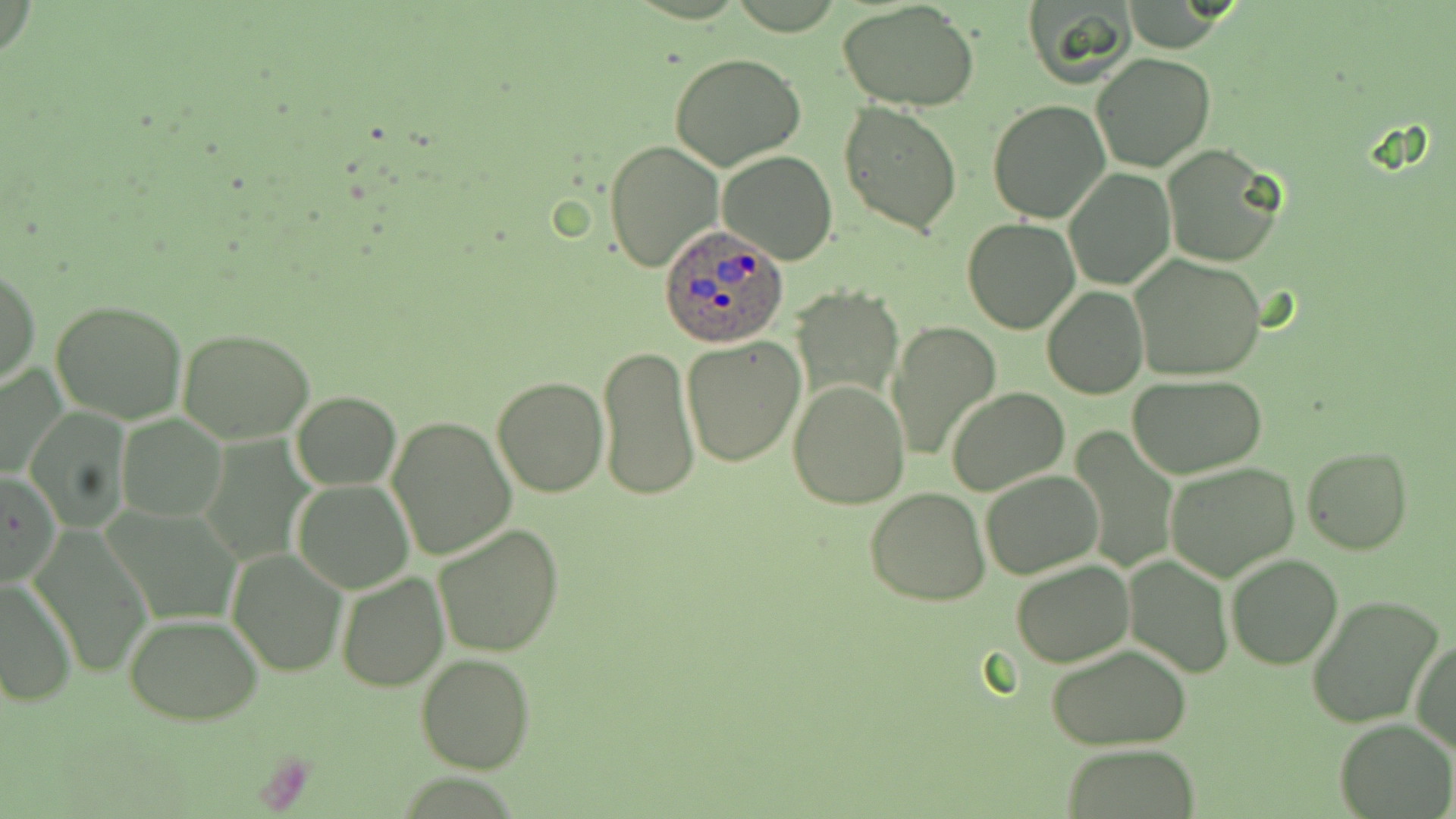

slide-level diagnosis = Plasmodium ovale
stain = May-Grünwald-Giemsa
image size = 1456×819 pixels
modality = light microscopy
uninfected red blood cell locations = approximate bounding boxes as (x1, y1, x2, y2) in pixels: (837, 0, 981, 113), (1020, 1, 1139, 89), (1091, 52, 1216, 173), (670, 54, 806, 171), (837, 100, 963, 236), (987, 100, 1110, 224), (604, 137, 724, 274), (1160, 145, 1280, 266), (716, 147, 838, 264), (1064, 169, 1175, 290), (961, 218, 1080, 334), (1129, 255, 1267, 381), (1, 264, 40, 390), (1043, 286, 1148, 399), (793, 290, 904, 408), (49, 298, 190, 423), (886, 320, 1003, 463), (178, 326, 314, 444), (680, 337, 804, 467), (597, 344, 699, 502), (0, 362, 67, 482), (1127, 373, 1268, 478), (492, 376, 608, 497), (786, 378, 910, 510), (947, 386, 1069, 496), (291, 391, 402, 490), (27, 412, 132, 528), (117, 414, 228, 522), (387, 416, 516, 560), (1066, 427, 1180, 574), (1301, 445, 1411, 554), (1163, 462, 1301, 582), (1, 469, 59, 588), (981, 469, 1104, 581), (293, 479, 414, 594), (865, 487, 991, 605), (105, 504, 240, 627), (432, 523, 565, 658), (28, 524, 154, 677), (225, 548, 348, 679), (1122, 554, 1233, 677), (1225, 554, 1343, 670), (1010, 560, 1133, 667), (335, 572, 449, 693), (0, 578, 77, 708), (1307, 597, 1442, 728), (124, 614, 263, 725), (1409, 637, 1455, 754), (1045, 644, 1194, 749), (416, 653, 534, 774), (1334, 718, 1454, 818), (1060, 743, 1204, 817)
Plasmodium ovale-infected red blood cell locations = approximate bounding boxes as (x1, y1, x2, y2) in pixels: (658, 222, 790, 348)
field of view = single
preparation = thin blood smear
magnification = 1000x